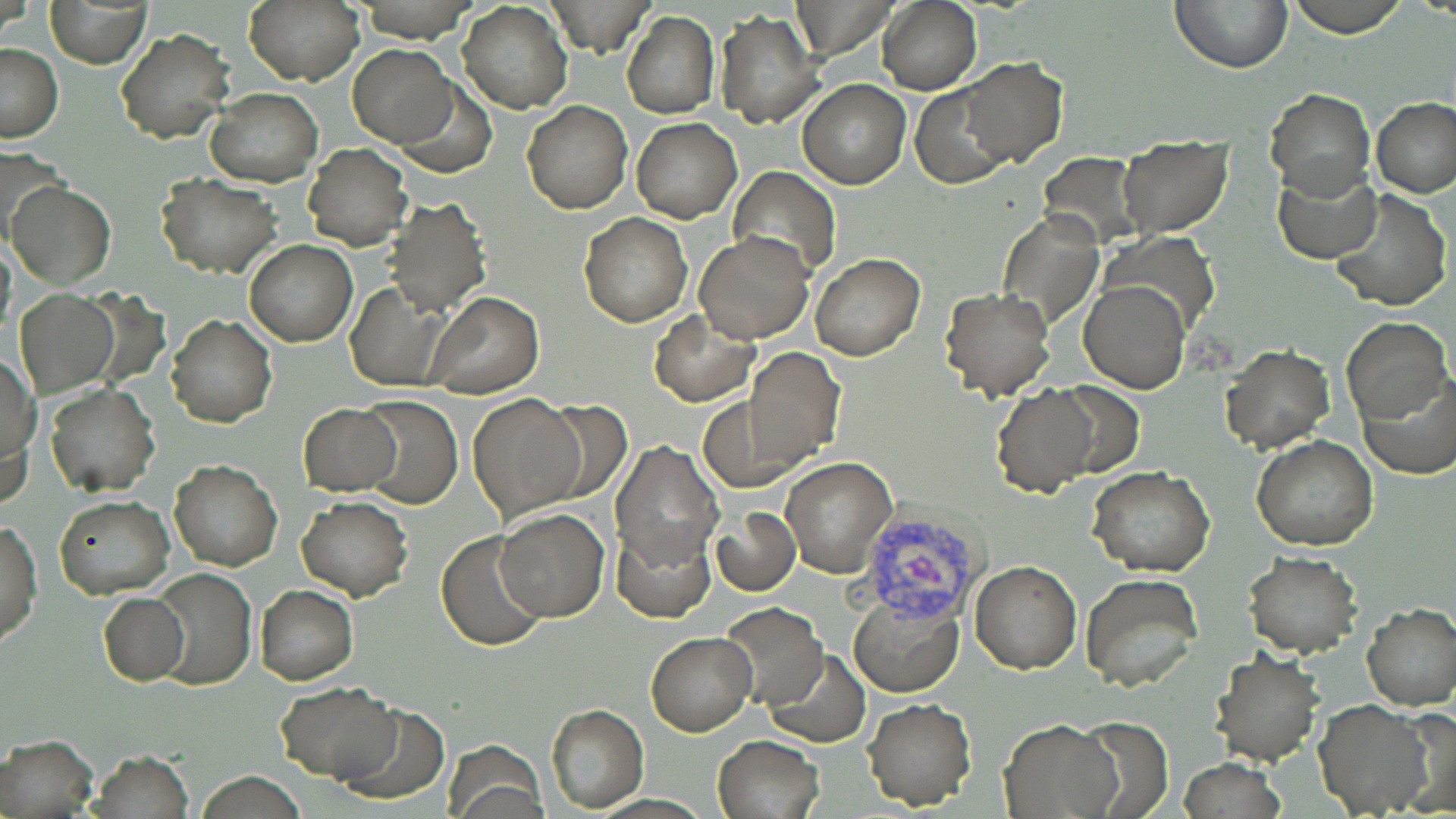
Approximate bounding boxes as (x1, y1, x2, y2) in pixels. Uninfected red blood cell locations: (244, 0, 363, 86), (544, 0, 654, 56), (1171, 0, 1292, 72), (1288, 0, 1408, 36), (45, 1, 151, 68), (458, 1, 573, 114), (878, 1, 981, 94), (715, 9, 824, 128), (623, 11, 719, 119), (115, 29, 235, 145), (0, 42, 63, 141), (348, 45, 458, 147), (958, 58, 1068, 167), (798, 78, 911, 190), (394, 84, 496, 177), (911, 86, 1015, 188), (204, 88, 323, 186), (1265, 88, 1374, 200), (1370, 97, 1455, 199), (522, 101, 633, 215), (632, 117, 742, 223), (1116, 137, 1232, 237), (304, 144, 412, 250), (0, 147, 67, 252), (1041, 151, 1146, 249), (1273, 165, 1382, 264), (729, 166, 841, 279), (156, 174, 282, 275), (6, 181, 116, 288), (1328, 186, 1451, 312), (385, 197, 492, 316), (997, 210, 1104, 327), (578, 212, 692, 328), (696, 231, 816, 344), (1101, 232, 1220, 335), (245, 240, 357, 346), (810, 252, 924, 360), (1079, 280, 1190, 394), (345, 282, 454, 393), (940, 288, 1054, 400), (15, 290, 119, 396), (425, 292, 542, 398), (648, 310, 760, 406), (167, 314, 277, 428), (1342, 317, 1453, 426), (1222, 343, 1333, 454), (744, 349, 845, 468), (2, 353, 41, 467), (1360, 375, 1456, 478), (1051, 381, 1143, 478), (45, 383, 159, 497), (993, 384, 1100, 498), (467, 392, 588, 521), (356, 396, 463, 509), (698, 396, 807, 492), (536, 400, 634, 505), (298, 404, 401, 494), (1, 412, 32, 516), (1251, 436, 1379, 551), (610, 438, 724, 570), (779, 457, 898, 577), (169, 459, 283, 571), (1088, 467, 1213, 577), (54, 496, 173, 600), (297, 497, 413, 601), (711, 506, 801, 595), (496, 508, 609, 621), (0, 519, 43, 644), (612, 520, 714, 621), (436, 530, 548, 651), (1243, 551, 1362, 657), (970, 561, 1081, 675), (151, 566, 256, 690), (1079, 574, 1204, 693), (255, 584, 358, 684), (98, 592, 188, 685), (849, 594, 964, 697), (719, 602, 828, 708), (1361, 602, 1456, 711), (647, 632, 756, 735), (763, 649, 871, 748), (1209, 652, 1326, 767), (276, 681, 399, 781), (862, 697, 976, 810), (1314, 699, 1436, 817), (335, 704, 448, 804), (545, 705, 648, 812), (1399, 706, 1456, 818), (1000, 719, 1123, 817), (1071, 719, 1173, 817), (0, 732, 99, 817), (713, 735, 824, 819), (443, 739, 548, 818), (90, 749, 193, 819), (1178, 759, 1287, 819), (198, 771, 308, 817). Plasmodium vivax-infected red blood cell locations: (846, 489, 987, 622). Platelet locations: (1185, 331, 1239, 377). Slide-level diagnosis: Plasmodium vivax. Single field of view. Optical microscopy. Thin blood smear. Image is 1456×819 pixels. May-Grünwald-Giemsa-stained preparation. 1000x magnification.